Classify this cell by malaria status.
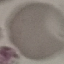
Uninfected.

Summary:
  - Preparation: thin smear
  - Image type: cell patch, automatically extracted from a larger field of view and resized to 64 × 64 pixels
  - Capture: smartphone camera at the microscope eyepiece
  - Stain: Giemsa